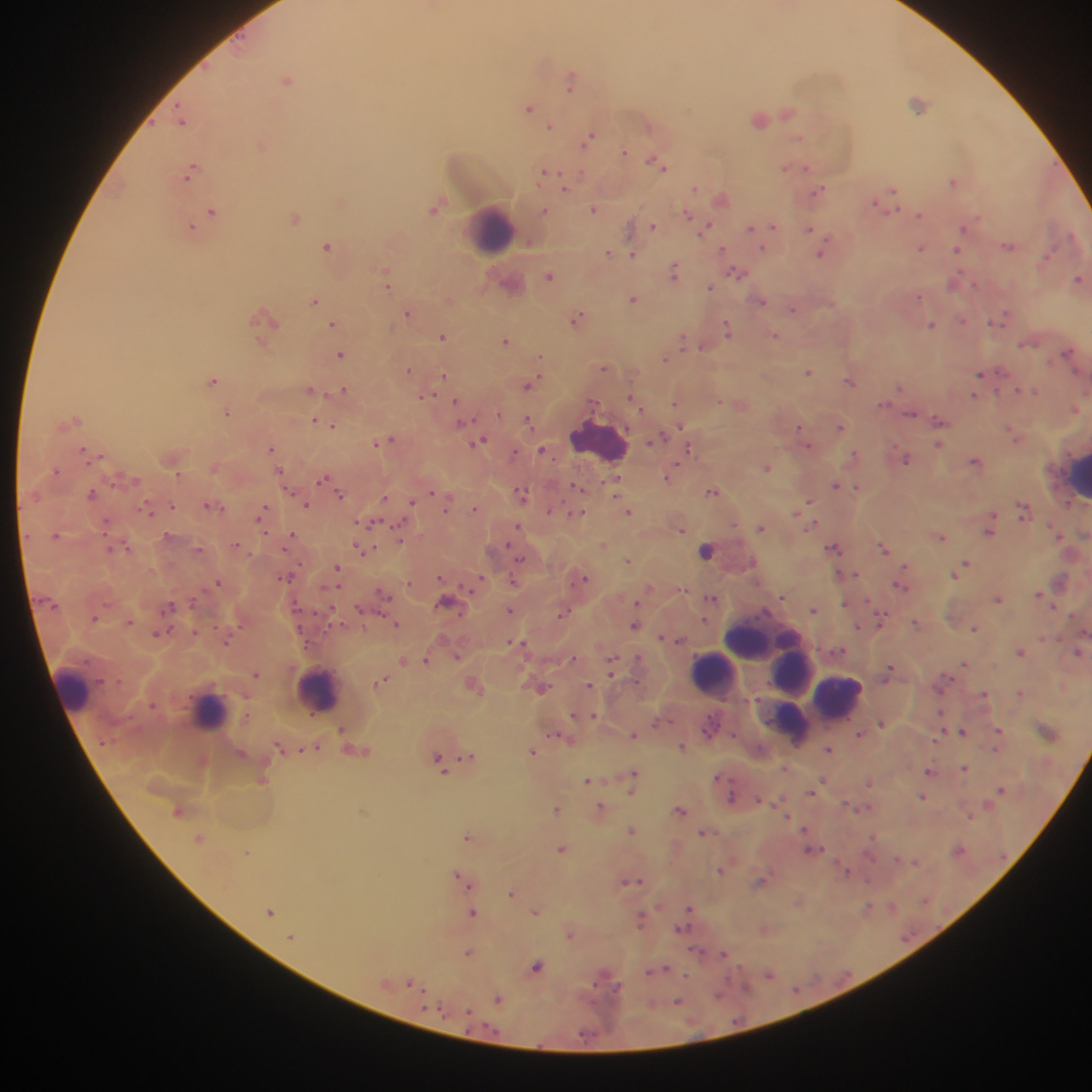

Approximate centers as (x, y) in pixels. Plasmodium parasite locations: (287, 79), (571, 79), (918, 103), (529, 108), (787, 112), (759, 119), (182, 122), (550, 126), (589, 138), (798, 138), (260, 145), (625, 152), (658, 162), (664, 167), (785, 168), (806, 169), (190, 170), (545, 171), (954, 181), (565, 187), (695, 188), (821, 190), (892, 190), (722, 198), (342, 202), (879, 203), (434, 208), (593, 209), (212, 211), (545, 211), (688, 214), (920, 215), (295, 218), (773, 225), (654, 226), (708, 226), (964, 226), (191, 227), (751, 228), (811, 228), (1007, 246), (327, 247), (921, 248), (723, 249), (763, 249), (957, 250), (608, 252), (633, 254), (820, 254), (1047, 256), (675, 271), (737, 272), (386, 274), (550, 276), (1077, 279), (952, 282), (976, 284), (387, 286), (710, 287), (919, 296), (633, 299), (761, 300), (314, 301), (831, 303), (793, 309), (408, 313), (1002, 317), (576, 318), (264, 319), (962, 320), (997, 321), (333, 323), (933, 326), (727, 329), (776, 335), (442, 337), (683, 339), (505, 340), (1025, 344), (702, 346), (1067, 354), (340, 355), (540, 358), (665, 358), (605, 367), (409, 369), (809, 372), (980, 374), (443, 376), (213, 381), (849, 381), (529, 385), (900, 387), (310, 389), (344, 389), (1018, 390), (1027, 391), (1036, 392), (975, 396), (425, 397), (631, 399), (456, 401), (720, 401), (675, 402), (883, 404), (1076, 409), (227, 413), (910, 414), (73, 420), (314, 420), (324, 421), (528, 421), (461, 422), (939, 422), (333, 425), (841, 427), (800, 428), (1013, 434), (660, 436), (385, 440), (804, 440), (481, 441), (939, 444), (807, 445), (271, 448), (84, 450), (541, 450), (688, 450), (514, 454), (854, 455), (907, 459), (975, 461), (767, 467), (55, 471), (279, 471), (178, 474), (668, 477), (323, 478), (836, 485), (577, 487), (617, 487), (858, 487), (712, 492), (92, 493), (431, 493), (522, 493), (341, 495), (385, 498), (810, 501), (412, 502), (212, 505), (307, 505), (171, 506), (447, 506), (474, 509), (149, 511), (551, 511), (628, 511), (1023, 511), (262, 512), (579, 514), (106, 523), (372, 523), (812, 525), (517, 527), (761, 527), (682, 529), (988, 531), (56, 535), (400, 537), (291, 538), (942, 538), (603, 544), (237, 545), (127, 546), (835, 547), (883, 547), (198, 548), (360, 549), (368, 549), (706, 550), (629, 560), (966, 565), (337, 568), (958, 571), (955, 575), (440, 577), (283, 578), (584, 578), (480, 579), (514, 579), (218, 582), (409, 582), (901, 585), (382, 594), (1038, 594), (783, 596), (712, 598), (998, 599), (446, 601), (192, 602), (845, 603), (170, 607), (359, 610), (511, 610), (813, 610), (562, 613), (94, 618), (881, 620), (129, 622), (915, 622), (396, 625), (634, 626), (858, 628), (975, 629), (158, 633), (663, 637), (225, 641), (515, 643), (1020, 652), (1078, 652), (457, 656), (572, 659), (403, 660), (427, 660), (964, 663), (611, 665), (889, 670), (256, 674), (381, 682), (589, 685), (474, 687), (542, 687), (1021, 692), (984, 694), (593, 715), (882, 723), (342, 729), (999, 730), (962, 731), (557, 734), (860, 734), (633, 736), (682, 747), (829, 750), (533, 751), (469, 756), (438, 761), (965, 768), (928, 770), (633, 776), (587, 781), (868, 782), (1002, 789), (731, 797), (923, 797), (759, 799), (557, 809), (600, 809), (680, 810), (633, 831), (703, 832), (467, 836), (873, 837), (199, 838), (959, 848), (561, 849), (812, 850), (247, 852), (915, 862), (721, 871), (846, 871), (457, 874), (464, 880), (632, 881), (760, 881), (469, 886), (511, 893), (893, 906), (868, 907), (688, 909), (270, 912), (535, 912), (472, 913), (641, 919), (570, 935), (291, 937), (469, 952), (724, 954), (537, 967), (659, 970), (770, 975), (411, 983), (498, 999), (678, 1001). Leukocyte locations: (491, 228), (599, 440), (1077, 476), (759, 637), (733, 659), (793, 672), (713, 673), (73, 687), (320, 688), (839, 695), (208, 712), (795, 716). Single field of view. Mobile-phone photograph taken through the microscope. Image is 1092×1092 pixels. Thick blood film. Collected in Ghana.